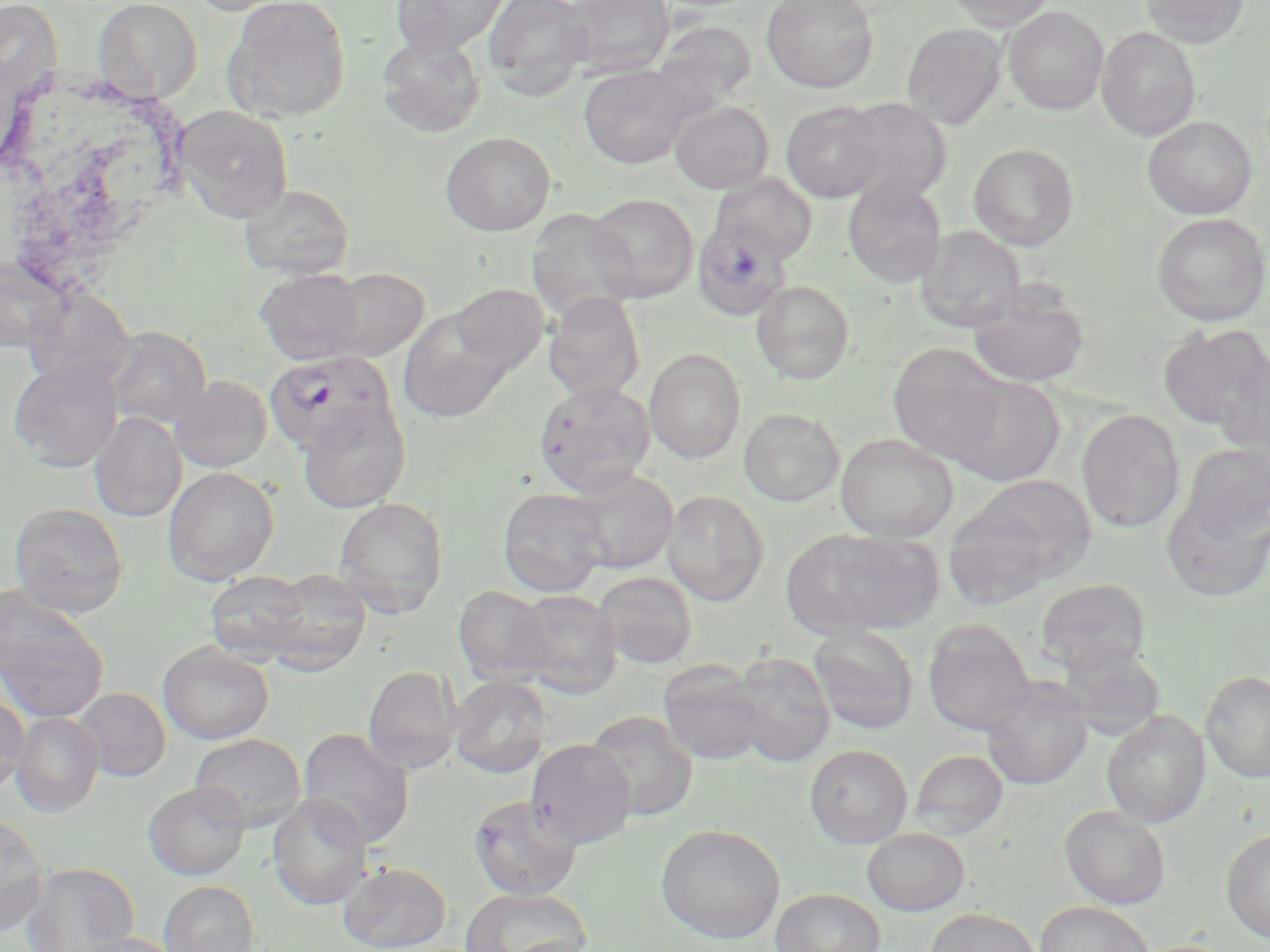
slide-level diagnosis = Plasmodium falciparum
image size = 1270×952 pixels
stain = May-Grünwald-Giemsa
field of view = single
preparation = thin blood smear
Plasmodium falciparum-infected red blood cell locations = approximate bounding boxes as (x1, y1, x2, y2) in pixels: (692, 217, 791, 324), (264, 351, 395, 457)
modality = optical microscopy
uninfected red blood cell locations = approximate bounding boxes as (x1, y1, x2, y2) in pixels: (93, 0, 203, 101), (183, 0, 297, 15), (222, 0, 351, 123), (390, 0, 509, 57), (481, 0, 592, 101), (560, 0, 674, 79), (761, 0, 879, 93), (946, 0, 1057, 31), (1139, 0, 1250, 47), (1003, 6, 1108, 116), (651, 20, 757, 117), (901, 23, 1008, 129), (1096, 27, 1200, 141), (376, 33, 486, 138), (578, 64, 695, 169), (838, 97, 952, 204), (670, 100, 773, 194), (781, 101, 886, 202), (174, 106, 293, 223), (1143, 116, 1257, 220), (440, 132, 556, 236), (968, 143, 1079, 250), (710, 173, 818, 263), (843, 180, 947, 287), (240, 184, 355, 279), (587, 193, 699, 303), (526, 208, 640, 324), (1151, 213, 1269, 326), (916, 226, 1026, 332), (0, 257, 69, 352), (255, 268, 369, 366), (325, 268, 429, 361), (751, 280, 855, 384), (966, 283, 1090, 388), (449, 284, 548, 373), (543, 292, 646, 403), (398, 308, 516, 422), (1157, 324, 1269, 433), (105, 327, 211, 430), (886, 342, 1012, 466), (644, 349, 746, 464), (1216, 349, 1270, 466), (9, 359, 122, 472), (169, 375, 273, 473), (942, 375, 1066, 486), (533, 381, 656, 497), (297, 399, 411, 514), (738, 407, 844, 506), (1076, 409, 1185, 533), (90, 412, 186, 522), (835, 434, 958, 542), (1177, 442, 1270, 545), (162, 466, 279, 585), (565, 469, 678, 573), (946, 474, 1096, 601), (497, 487, 610, 597), (1161, 489, 1270, 603), (662, 490, 769, 606), (332, 497, 449, 617), (9, 502, 129, 617), (784, 528, 943, 638), (205, 570, 314, 662), (260, 570, 372, 675), (593, 571, 698, 669), (1035, 579, 1151, 676), (453, 585, 555, 686), (0, 586, 108, 723), (514, 590, 622, 698), (922, 620, 1035, 737), (808, 626, 919, 735), (157, 641, 274, 745), (1054, 644, 1166, 739), (729, 651, 835, 767), (658, 660, 765, 765), (363, 665, 461, 772), (1201, 670, 1270, 783), (449, 675, 553, 779), (980, 676, 1093, 790), (73, 687, 171, 782), (0, 694, 29, 796), (10, 711, 104, 817), (585, 711, 697, 821), (1102, 711, 1210, 828), (297, 727, 415, 848), (190, 733, 306, 830), (526, 739, 637, 849), (804, 744, 913, 848), (909, 750, 1008, 840), (142, 781, 251, 881), (268, 793, 374, 910), (467, 794, 584, 900), (1060, 805, 1170, 909), (0, 810, 49, 935), (655, 824, 784, 944), (862, 828, 970, 916), (1221, 828, 1270, 943), (20, 862, 139, 952), (338, 862, 451, 951), (158, 880, 260, 952), (459, 888, 591, 952), (771, 888, 885, 952), (1034, 901, 1154, 952), (924, 907, 1041, 952), (66, 934, 184, 952)
magnification = 1000x